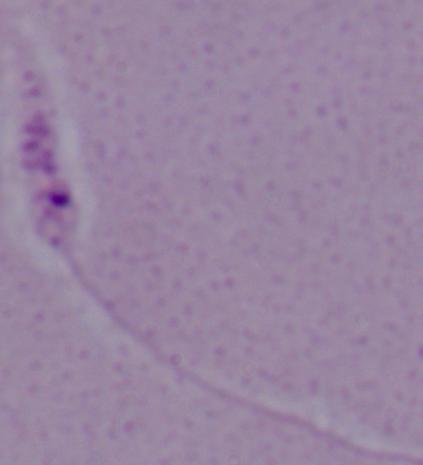
Captured at 1000x magnification. A Leishmania parasite is seen. Micrograph.